State which cell type is depicted.
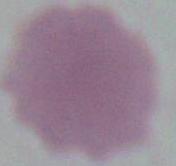

An erythrocyte.

Photomicrograph. Captured at 1000x magnification.